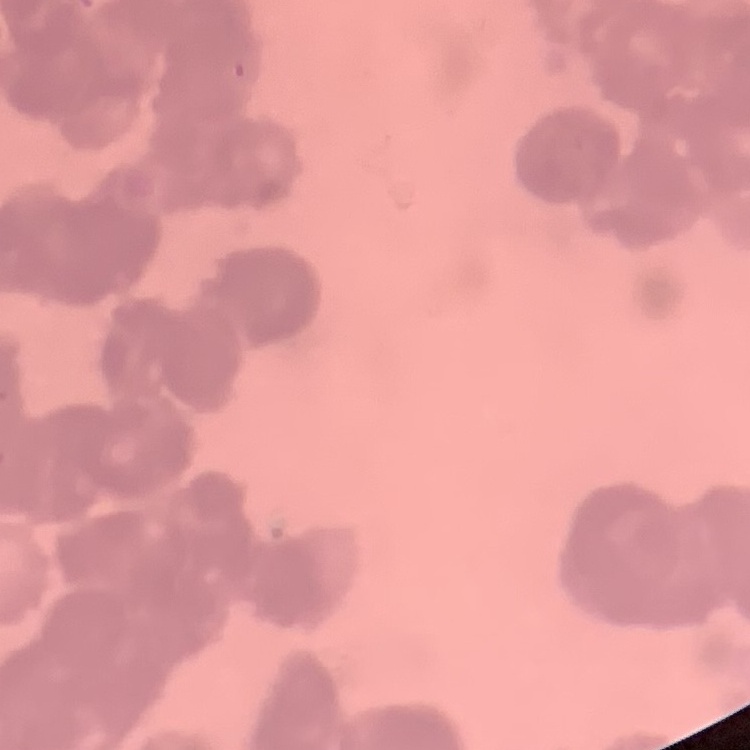 The erythrocytes exhibit rouleaux formation. One tile cut from a larger photomicrograph. Thin peripheral smear. Stained with either Field's or Giemsa.